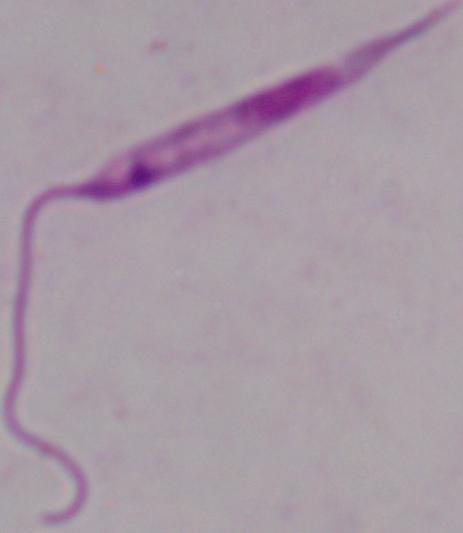
Summary:
  - Modality: photomicrograph
  - Magnification: 1000x
  - Identification: Leishmania